Outline each blood parasite and name the species.
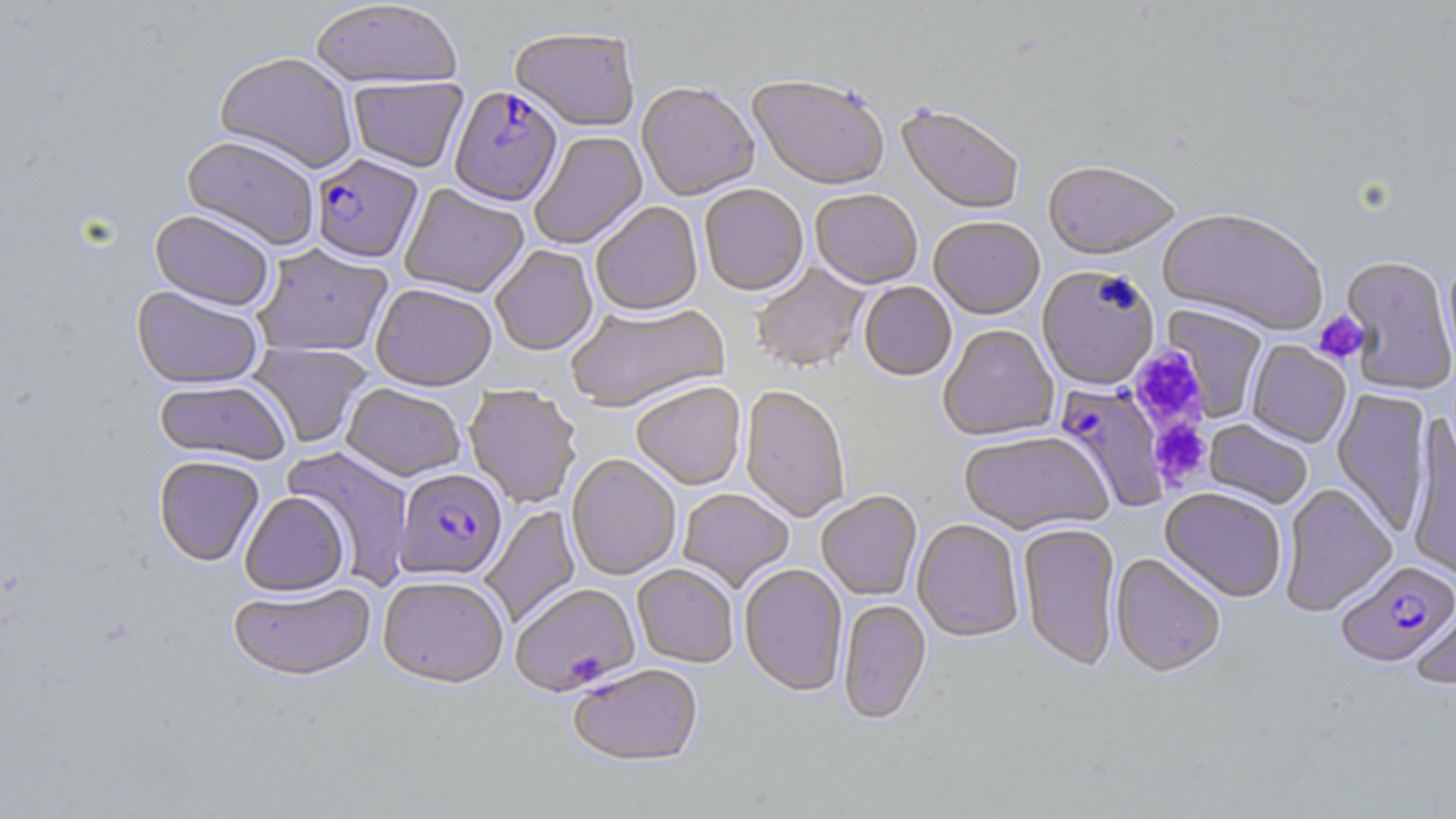

Approximate bounding boxes as (x1,y1)-(x2,y2) corner pairs in pixels.
Plasmodium falciparum-infected red blood cells (subset): (449,88)-(562,208), (311,155)-(424,266), (1053,382)-(1170,512), (395,468)-(507,580), (1335,560)-(1456,668).
No Plasmodium ovale, Plasmodium malariae, Plasmodium vivax, Babesia divergens, or Trypanosoma brucei observed.

Summary:
  - Uninfected red blood cell locations (subset): (310,2)-(462,92), (510,30)-(639,134), (213,53)-(358,174), (348,77)-(468,174), (747,78)-(889,193), (636,84)-(759,202), (896,105)-(1024,216), (529,131)-(648,251), (181,136)-(319,252), (1042,164)-(1180,264), (398,184)-(529,299), (699,185)-(809,298), (810,191)-(922,291), (591,203)-(703,319), (149,210)-(275,312), (1158,211)-(1328,338), (929,218)-(1045,321), (252,245)-(393,358), (491,246)-(598,357), (1443,254)-(1456,373), (1338,256)-(1455,394), (751,262)-(870,374), (1037,268)-(1159,391), (859,283)-(957,383), (371,285)-(496,393), (132,286)-(263,390), (565,303)-(731,415), (1162,305)-(1268,422), (938,326)-(1058,443), (1246,341)-(1351,448), (247,342)-(373,449), (155,379)-(290,465), (631,383)-(746,492), (341,384)-(466,482), (463,386)-(581,508), (739,386)-(850,523), (1332,388)-(1434,538), (1406,414)-(1456,583), (1203,419)-(1313,509), (958,432)-(1112,536), (282,445)-(414,588), (566,454)-(681,581), (153,456)-(264,567), (1280,483)-(1397,617), (1160,488)-(1286,602), (677,489)-(794,593), (239,492)-(349,598), (816,492)-(922,601), (480,505)-(581,628), (912,519)-(1024,644), (1018,523)-(1121,672), (1110,553)-(1226,680), (632,564)-(738,669), (738,565)-(848,698), (377,577)-(509,690), (229,584)-(375,684), (1410,593)-(1456,692), (838,600)-(932,726), (568,665)-(703,769)
  - Platelet locations: (1312,310)-(1370,365), (1131,350)-(1209,430), (1149,418)-(1211,489)
  - Slide-level diagnosis: Plasmodium falciparum
  - Image size: 1456×819 pixels
  - Magnification: 1000x
  - Stain: May-Grünwald-Giemsa
  - Modality: light microscopy
  - Field of view: single
  - Preparation: thin blood smear